Comment on the morphology of the red blood cells.
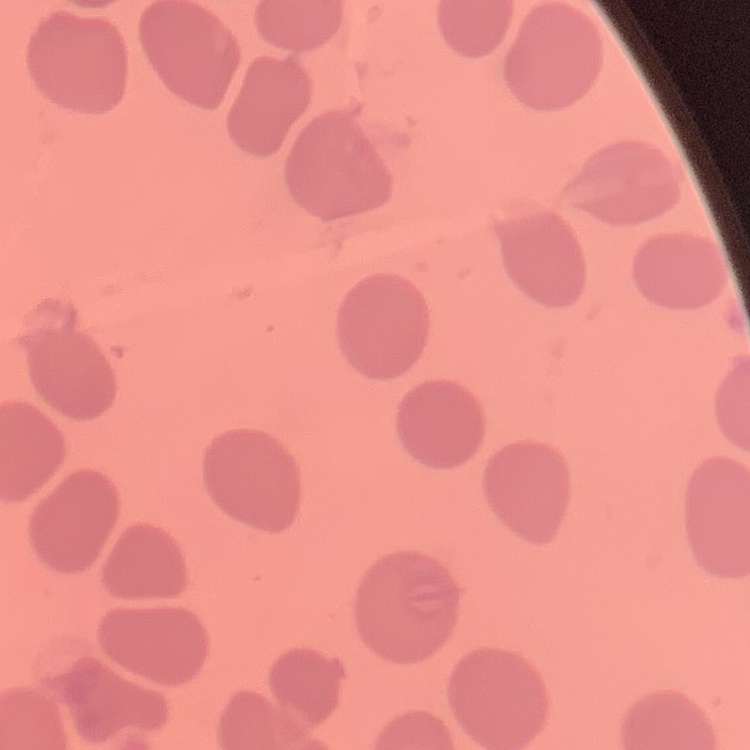
No rouleaux formation.

One tile cut from a larger photomicrograph. Thin peripheral smear. Stained with either Field's or Giemsa.